Give the position of every malaria parasite.
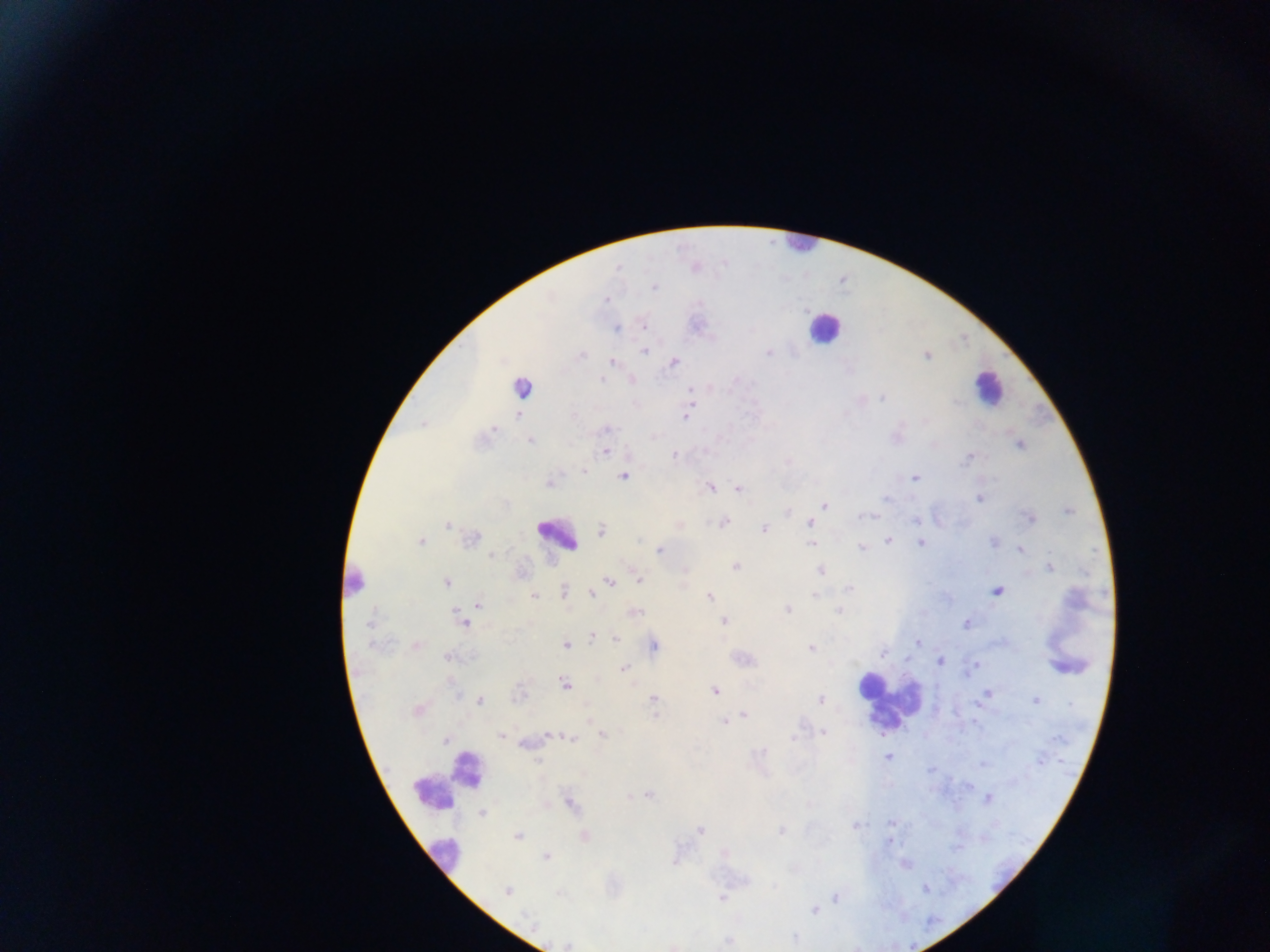

Approximate centers as x y in pixels.
Malaria parasites: 620 269; 654 289; 606 300; 616 329; 644 352; 768 353; 583 354; 928 356; 611 361; 673 362; 601 378; 631 379; 688 388; 521 389; 691 391; 883 398; 693 403; 517 411; 519 416; 686 418; 423 424; 494 429; 607 429; 529 440; 1020 445; 606 451; 673 454; 970 457; 582 471; 623 476; 915 479; 710 488; 738 488; 886 498; 978 499; 824 505; 1069 512; 860 517; 1031 518; 916 521; 724 522; 809 522; 447 526; 764 528; 601 531; 474 536; 558 537; 888 541; 421 542; 568 542; 920 543; 994 543; 811 544; 574 546; 862 549; 659 550; 1021 550; 493 556; 735 566; 1051 568; 821 571; 640 581; 448 582; 610 582; 354 584; 564 589; 849 590; 997 592; 591 593; 813 595; 534 596; 710 596; 479 605; 787 609; 838 611; 724 620; 464 624; 965 624; 369 625; 592 635; 616 639; 917 640; 565 644; 371 646; 417 646; 654 647; 412 648; 812 648; 883 653; 447 656; 940 661; 625 668; 563 684; 714 691; 652 698; 820 699; 1036 701; 480 702; 418 710; 743 716; 724 722; 823 733; 602 734; 548 735; 501 736; 571 738; 793 740; 447 741; 761 751; 887 757; 539 760; 649 794; 988 800; 569 802; 480 815; 891 824; 855 827; 700 830; 782 830; 517 836; 584 836; 889 840; 545 857; 774 886; 925 890; 507 891; 559 894; 835 898; 721 899; 815 910; 796 937; 728 942.

Leukocyte locations: 796 247; 820 332; 987 396; 885 704; 443 786; 441 858. Thick blood film. Image is 1270×952 pixels. Collected in Ghana. One field of view. Photographed through a microscope with a mobile-phone camera.